Identify the parasite.
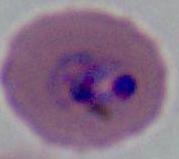
This is Plasmodium.

Summary:
  - Magnification: 400x or 1000x
  - Modality: photomicrograph